Identify the blood parasite species.
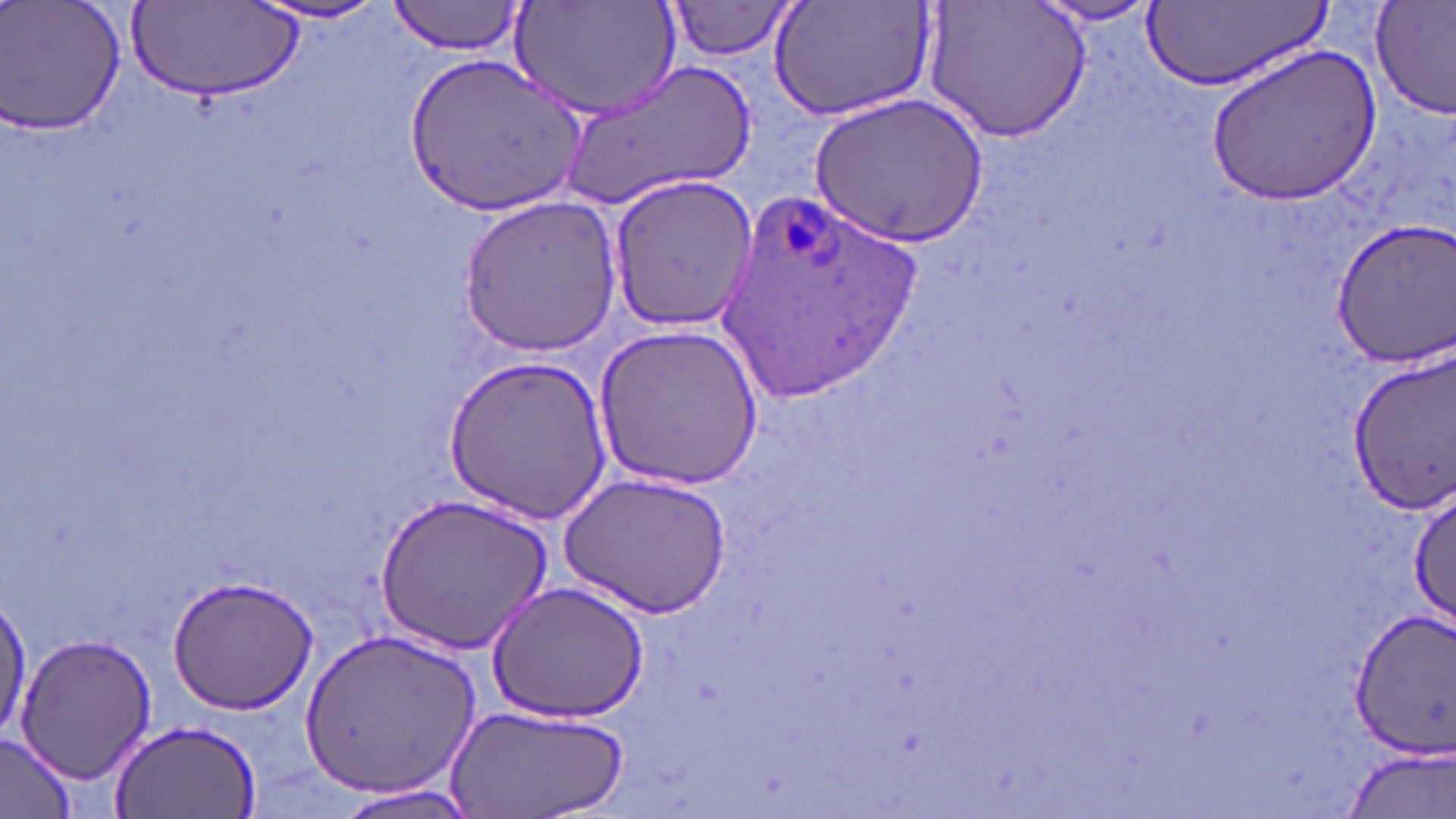

Plasmodium ovale.

Approximate bounding boxes as (x1, y1, x2, y2) in pixels. Plasmodium ovale-infected red blood cell locations: (715, 184, 931, 400). Uninfected red blood cell locations: (0, 0, 126, 140), (389, 0, 527, 56), (1031, 0, 1166, 28), (1145, 0, 1332, 94), (250, 1, 395, 26), (767, 1, 937, 123), (926, 1, 1092, 143), (1368, 1, 1456, 120), (510, 2, 682, 122), (665, 2, 801, 60), (132, 4, 301, 106), (1207, 45, 1380, 206), (403, 52, 589, 216), (562, 57, 757, 213), (807, 89, 989, 248), (605, 175, 762, 334), (456, 196, 622, 358), (1330, 220, 1456, 367), (593, 323, 764, 492), (1346, 348, 1455, 516), (444, 355, 612, 525), (558, 471, 731, 620), (1410, 487, 1455, 633), (375, 494, 551, 656), (165, 574, 319, 714), (486, 580, 651, 721), (1, 588, 30, 747), (1345, 605, 1456, 755), (297, 627, 481, 800), (14, 631, 157, 785), (448, 702, 626, 818), (109, 716, 263, 819), (0, 734, 77, 818), (1339, 747, 1455, 818), (330, 781, 483, 818). May-Grünwald-Giemsa stain. Thin blood smear. Single field of view. Image is 1456×819 pixels. 1000x magnification. Optical microscopy.